Report the malaria status of this cell.
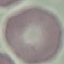

It is uninfected.

Summary:
  - Capture: smartphone through the microscope eyepiece
  - Preparation: thin blood smear
  - Stain: Giemsa
  - Image type: cell patch, automatically extracted from a larger field of view and resized to 64 × 64 pixels